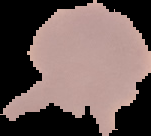
preparation = thin blood film
image type = segmented cell region on a black background
image size = 151×136 pixels
result = negative for Plasmodium parasites